Report the malaria status of this cell.
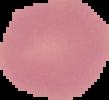
Uninfected.

Summary:
  - Image type: segmented cell region on a black background
  - Image size: 109×100 pixels
  - Preparation: thin blood film